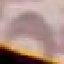 Result: no malaria parasites detected. Automatically extracted cell patch, resized to 64 × 64 pixels. Thin blood smear. Acquired by smartphone through the microscope eyepiece. Giemsa-stained preparation.